Name the blood parasite species.
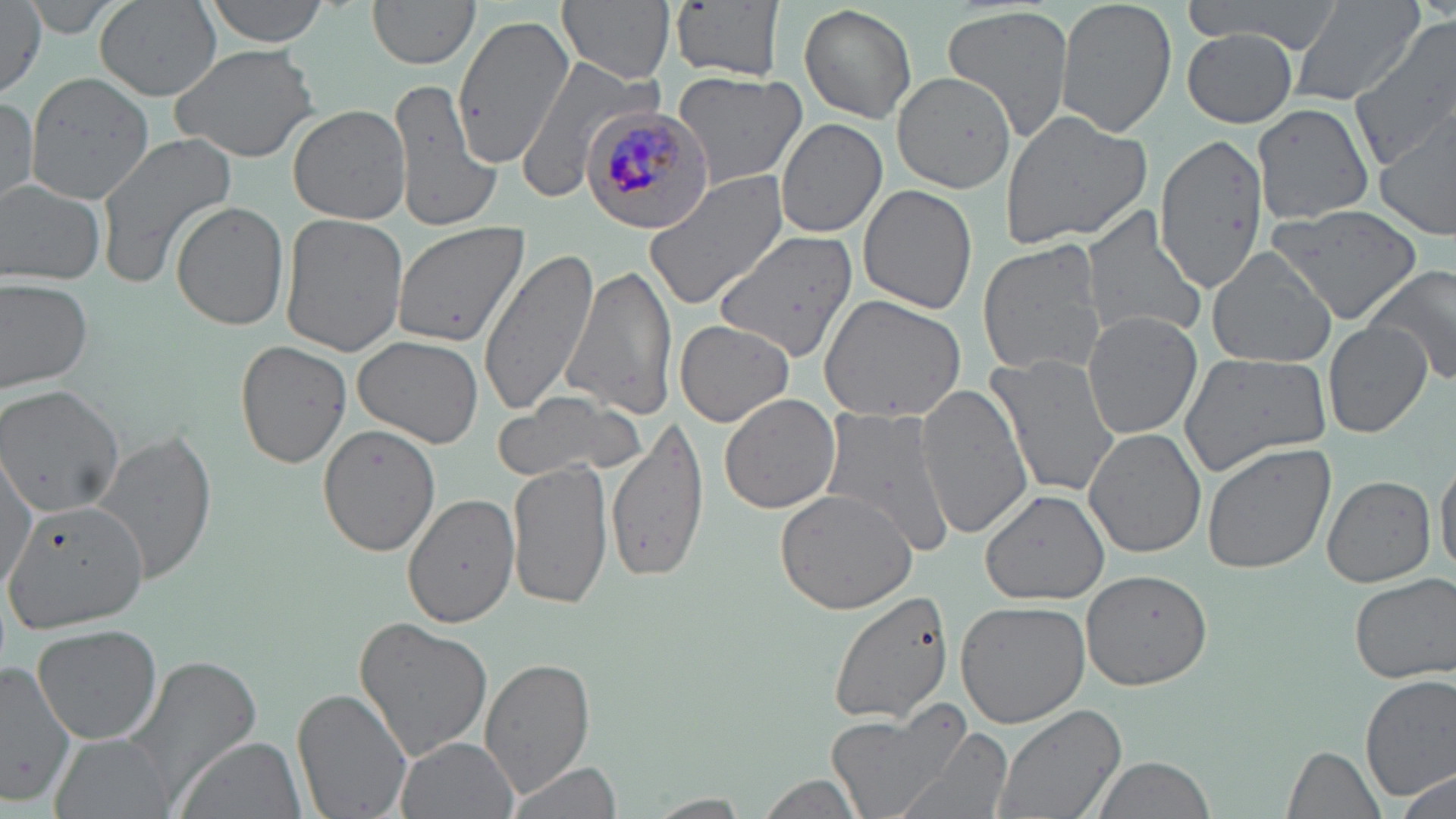

Plasmodium malariae.

Approximate bounding boxes as (x1,y1)-(x2,y2) corner pairs in pixels. Plasmodium malariae-infected red blood cell locations: (580,104)-(716,235). Uninfected red blood cell locations: (202,0)-(332,46), (367,0)-(481,71), (558,0)-(678,84), (1055,0)-(1177,139), (1181,0)-(1346,53), (1289,0)-(1423,106), (94,1)-(221,101), (0,2)-(48,102), (22,2)-(128,43), (671,2)-(786,83), (799,4)-(917,123), (942,5)-(1076,146), (451,14)-(576,170), (1352,22)-(1456,168), (1180,28)-(1303,126), (171,42)-(321,164), (512,54)-(651,204), (671,69)-(807,188), (24,72)-(154,205), (893,72)-(1017,191), (385,74)-(500,234), (0,93)-(39,208), (1252,102)-(1376,226), (288,103)-(412,225), (997,110)-(1155,252), (1374,112)-(1456,238), (774,118)-(886,239), (95,131)-(239,286), (1155,133)-(1268,291), (644,173)-(789,309), (0,181)-(106,284), (858,185)-(978,316), (171,202)-(289,331), (1263,203)-(1423,328), (1082,205)-(1207,344), (278,213)-(408,358), (388,220)-(530,351), (713,228)-(860,362), (977,240)-(1107,378), (477,244)-(603,418), (1206,247)-(1338,369), (565,261)-(679,422), (1367,265)-(1456,388), (0,276)-(94,394), (821,294)-(969,425), (1082,312)-(1203,439), (673,317)-(799,427), (1322,321)-(1433,438), (354,336)-(483,447), (235,339)-(352,469), (1175,349)-(1333,476), (985,353)-(1120,501), (917,385)-(1031,538), (0,386)-(128,517), (494,391)-(643,481), (719,393)-(842,514), (820,406)-(958,559), (608,419)-(711,584), (316,422)-(441,556), (1083,427)-(1204,558), (89,430)-(219,585), (1202,441)-(1336,576), (1,447)-(37,598), (1435,455)-(1456,579), (509,458)-(614,610), (1322,474)-(1436,587), (774,485)-(919,614), (981,486)-(1109,604), (4,491)-(153,632), (402,494)-(520,629), (1079,570)-(1216,692), (1348,572)-(1455,684), (825,589)-(954,726), (955,600)-(1091,727), (353,616)-(495,762), (31,624)-(164,747), (120,653)-(263,807), (0,656)-(81,806), (480,657)-(595,795), (1359,672)-(1456,801), (294,684)-(416,819), (991,703)-(1125,819), (828,704)-(969,819), (892,728)-(1013,819), (49,733)-(177,819), (174,734)-(305,819), (395,735)-(519,819), (1283,743)-(1384,817), (1090,754)-(1216,819), (503,762)-(624,816), (1392,768)-(1453,815), (753,772)-(869,818), (645,794)-(754,817). 1000x magnification. Thin blood smear. One field of a larger specimen. Optical microscopy. Image is 1456×819 pixels. May-Grünwald-Giemsa-stained preparation.